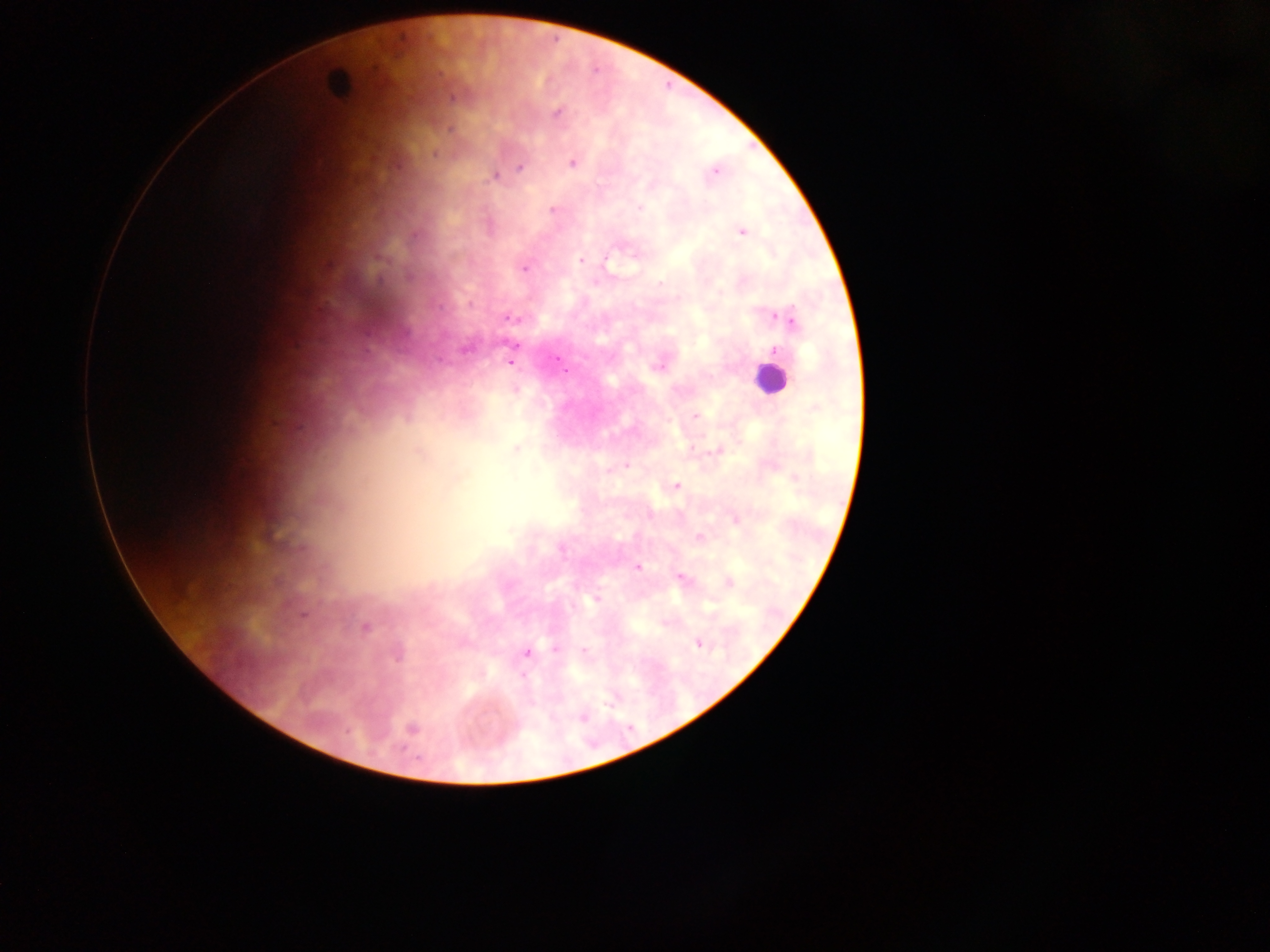

leukocyte locations = approximate centers as {x, y} in pixels: {338, 84}, {769, 378}
field of view = single
Plasmodium parasite locations = approximate centers as {x, y} in pixels: {556, 112}, {573, 163}, {519, 166}, {716, 172}, {493, 177}, {640, 207}, {553, 210}, {742, 232}, {581, 261}, {525, 269}, {660, 284}, {719, 292}, {512, 318}, {787, 318}, {776, 350}, {558, 360}, {510, 361}, {659, 365}, {680, 390}, {696, 415}, {517, 449}, {692, 449}, {716, 452}, {625, 466}, {676, 486}, {735, 519}, {699, 538}, {561, 549}, {638, 567}, {681, 577}, {730, 583}, {595, 599}, {664, 623}, {365, 627}, {699, 644}, {555, 649}, {584, 651}, {527, 652}, {522, 675}, {582, 718}
preparation = thick blood film
image size = 1270×952 pixels
capture = mobile-phone photograph through a microscope
country = Ghana